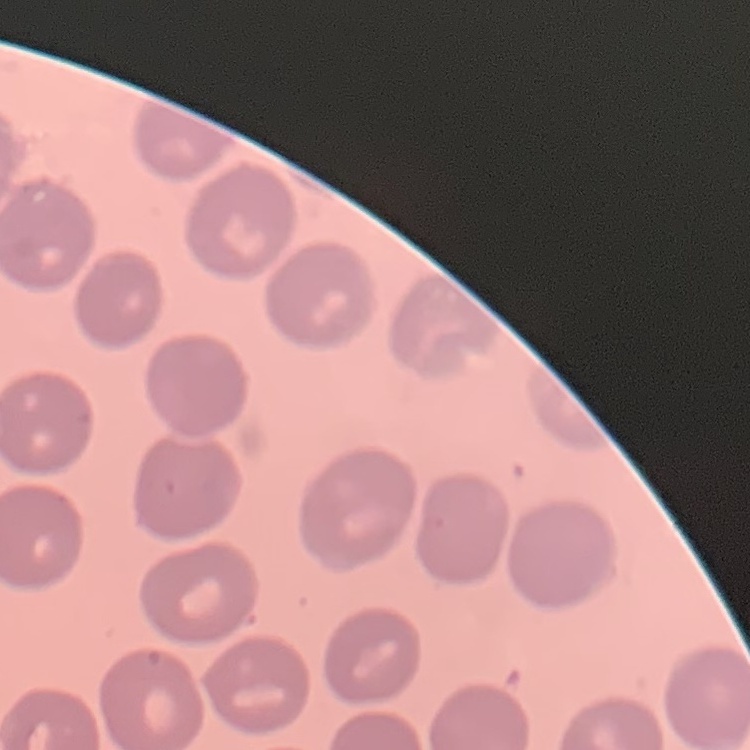

erythrocyte_morphology: no rouleaux formation
stain: Field's or Giemsa
image_type: square crop of a larger photomicrograph
preparation: thin blood smear